Classify this cell by malaria status.
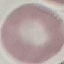
It is uninfected.

Summary:
  - Image type: automatically extracted cell patch, resized to 64 × 64 pixels
  - Stain: Giemsa
  - Preparation: thin blood film
  - Capture: smartphone camera at the microscope eyepiece